Classify this cell by malaria status.
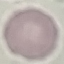
Uninfected.

Giemsa-stained preparation. Photographed with a smartphone camera at the microscope eyepiece. Thin blood smear. Cell patch, automatically extracted from a larger field of view and resized to 64 × 64 pixels.